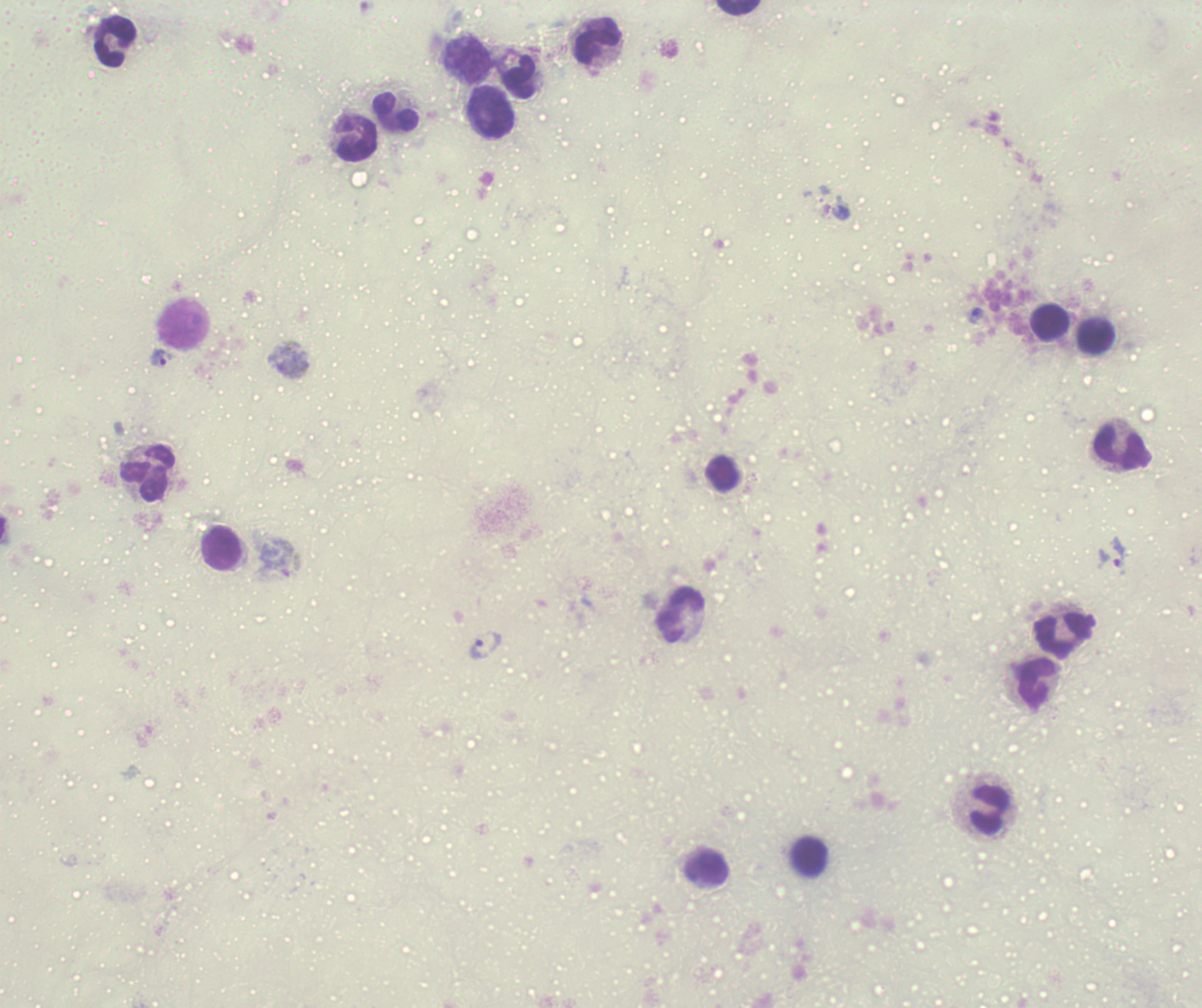

Approximate centers as {x, y} in pixels.
Summary:
  - Trophozoite locations: {976, 315}, {159, 358}, {1118, 552}, {484, 645}
  - Leukocyte locations: {739, 8}, {115, 41}, {599, 43}, {469, 62}, {521, 78}, {491, 112}, {396, 114}, {356, 137}, {1049, 321}, {1096, 337}, {1123, 449}, {147, 473}, {722, 475}, {222, 549}, {681, 614}, {1064, 636}, {1038, 685}, {990, 809}, {811, 856}, {707, 867}
  - Gametocyte locations: {281, 559}
  - Life-cycle stages observed: trophozoite, gametocyte
  - Magnification: 100x
  - Context: previously used in an actual diagnosis
  - Stain: Romanowsky
  - Result: malaria parasites detected
  - Preparation: thick smear of blood
  - Image size: 1202×1008 pixels
  - Field of view: single
  - Coloration quality: bad
  - Background quality: unsatisfactory